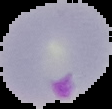
image type = segmented cell region on a black background
malaria status = parasitized
image size = 112×109 pixels
preparation = thin blood film